Classify this cell by malaria status.
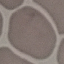

Uninfected.

Summary:
  - Stain: Giemsa
  - Capture: smartphone through the microscope eyepiece
  - Preparation: thin blood smear
  - Image type: automatically extracted cell patch, resized to 64 × 64 pixels